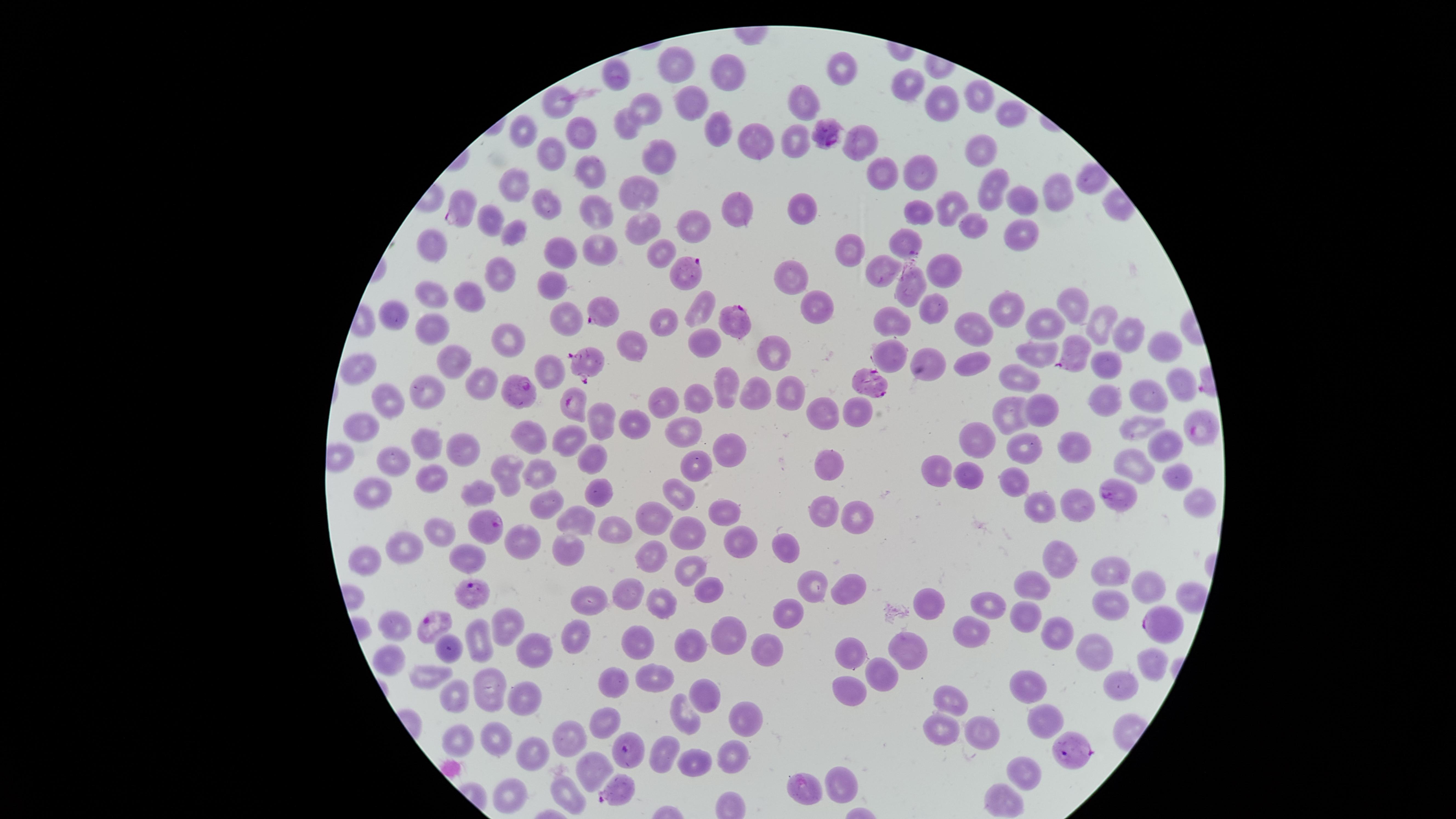

{
  "field_of_view": "single",
  "visible_region": "circular",
  "capture": "smartphone photograph through the microscope eyepiece",
  "stain": "Giemsa",
  "parasitized_RBCs": "approximate marker points as [x, y] in pixels: [830, 134], [458, 212], [691, 272], [597, 316], [738, 323], [1068, 350], [587, 364], [872, 384], [519, 390], [572, 404], [1197, 427], [1120, 497], [484, 527], [475, 591], [436, 623], [1157, 627], [625, 749], [1071, 750], [619, 788]",
  "species": "Plasmodium falciparum",
  "uninfected_RBCs": "approximate marker points as [x, y] in pixels: [676, 58], [845, 64], [728, 71], [616, 72], [907, 83], [979, 96], [691, 97], [804, 97], [557, 99], [937, 105], [645, 109], [1010, 111], [628, 125], [714, 126], [525, 130], [583, 132], [796, 132], [859, 139], [750, 140], [552, 149], [981, 149], [660, 154], [874, 166], [589, 167], [921, 174], [515, 184], [988, 187], [1057, 187], [640, 189], [1024, 197], [548, 202], [957, 205], [599, 207], [736, 208], [919, 208], [801, 209], [490, 217], [971, 220], [1018, 225], [515, 227], [697, 228], [649, 230], [906, 238], [599, 240], [431, 244], [660, 248], [848, 248], [559, 252], [949, 267], [497, 271], [884, 271], [793, 275], [909, 283], [549, 287], [471, 293], [433, 300], [703, 300], [818, 301], [1005, 302], [929, 304], [1069, 304], [394, 311], [562, 317], [896, 317], [1098, 317], [661, 324], [1043, 326], [972, 327], [1126, 327], [426, 332], [510, 333], [633, 340], [698, 343], [1162, 347], [778, 350], [888, 350], [1034, 351], [931, 355], [451, 356], [974, 361], [1108, 365], [550, 368], [362, 369], [1023, 379], [1184, 379], [479, 380], [725, 385], [423, 389], [758, 389], [784, 390], [1150, 393], [1103, 394], [692, 395], [664, 399], [389, 401], [820, 408], [855, 410], [1041, 410], [1014, 411], [598, 416], [633, 417], [365, 424], [1143, 424], [676, 431], [983, 432], [534, 435], [572, 439], [428, 440], [1077, 441], [1024, 444], [466, 447], [1164, 447], [733, 451], [390, 457], [593, 458], [1135, 461], [829, 463], [942, 464], [697, 465], [514, 468], [539, 469], [433, 472], [1168, 476], [964, 477], [1011, 479], [369, 488], [483, 492], [598, 492], [679, 496], [1196, 497], [546, 499], [1037, 503], [1076, 505], [822, 507], [724, 508], [579, 512], [858, 514], [655, 519], [439, 530], [609, 533], [679, 534], [735, 538], [782, 539], [519, 543], [402, 545], [572, 549], [465, 550], [654, 556], [1056, 556], [371, 559], [691, 567], [1110, 569], [1149, 583], [805, 584], [1034, 584], [634, 588], [848, 588], [706, 590], [1106, 599], [933, 600], [589, 601], [988, 601], [661, 607], [787, 611], [1026, 617], [511, 623], [395, 624], [1054, 626], [723, 629], [479, 637], [966, 637], [571, 638], [641, 640], [445, 641], [852, 645], [686, 647], [533, 648], [911, 649], [1091, 649], [767, 650], [389, 660], [429, 668], [881, 669], [661, 674], [1030, 679], [847, 683], [1118, 683], [614, 686], [487, 690], [701, 690], [950, 692], [529, 696], [453, 698], [683, 709], [744, 714], [1045, 720], [606, 723], [942, 723], [981, 727], [457, 736], [495, 736], [572, 737], [535, 749], [665, 749], [730, 754], [691, 762], [592, 766], [1021, 767], [841, 780], [505, 783], [565, 791], [808, 793], [1001, 797]",
  "presence": "malaria parasites detected",
  "image_size": "1456×819 pixels",
  "preparation": "thin blood film"
}